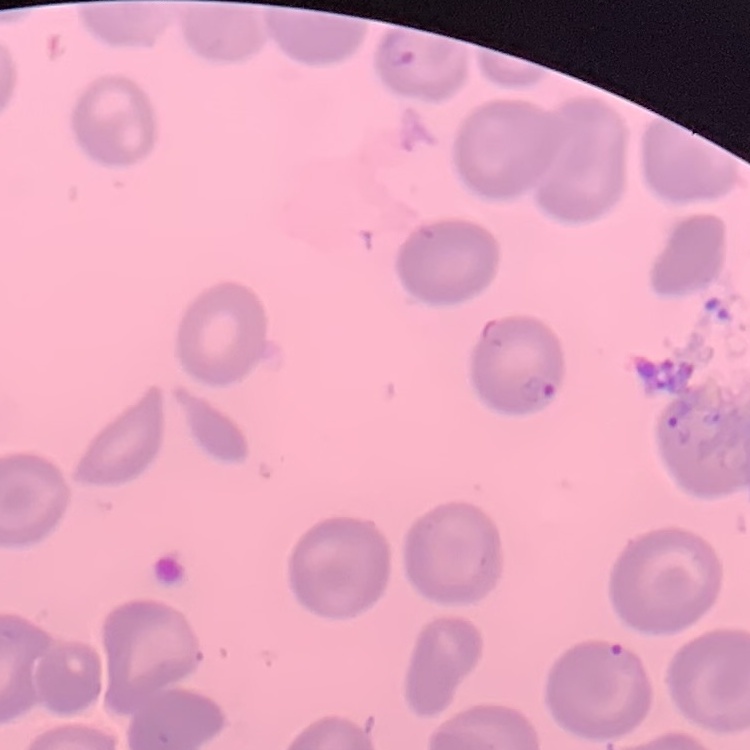

The red blood cells exhibit no rouleaux formation. Thin peripheral smear. Square crop of a larger photomicrograph. Field's or Giemsa stain.